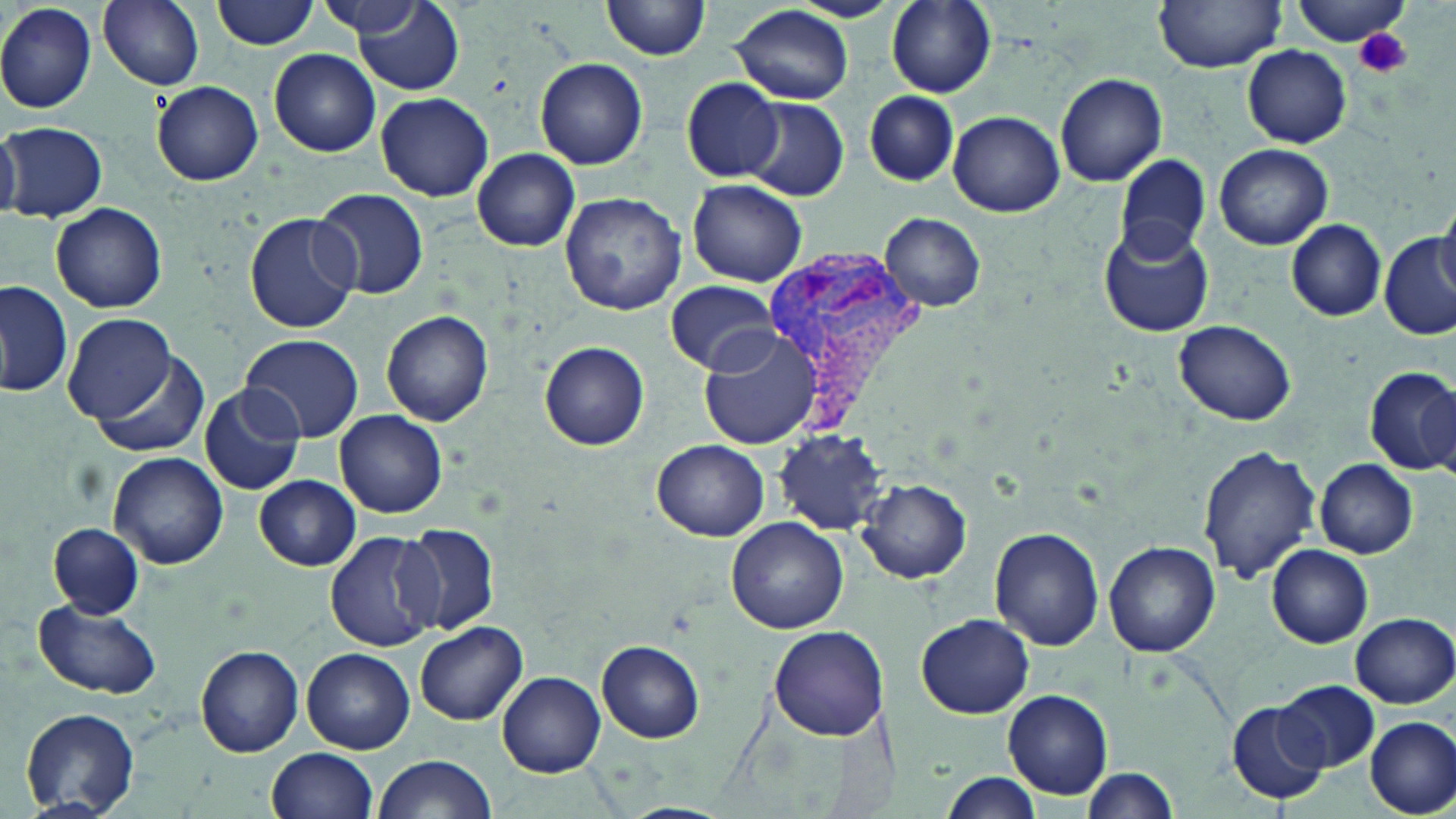

Summary:
  - Coordinate format: approximate bounding boxes as (x1,y1)-(x2,y2) corner pairs in pixels
  - Platelet locations: (1355,26)-(1411,78)
  - Uninfected red blood cell locations: (98,0)-(204,90), (213,0)-(318,50), (603,0)-(713,61), (885,0)-(996,98), (1154,0)-(1286,71), (1292,0)-(1414,47), (874,1)-(975,183), (0,2)-(97,113), (317,2)-(430,38), (352,3)-(464,97), (729,5)-(855,106), (1244,46)-(1351,147), (270,49)-(381,158), (535,57)-(647,169), (1055,72)-(1168,186), (681,78)-(784,181), (153,81)-(263,185), (376,92)-(493,201), (866,92)-(956,186), (741,99)-(848,200), (950,110)-(1064,216), (0,121)-(21,223), (2,122)-(108,223), (1213,143)-(1332,250), (471,148)-(580,251), (1117,154)-(1210,260), (687,179)-(807,287), (312,187)-(430,300), (561,193)-(687,316), (50,203)-(167,313), (1434,205)-(1456,303), (243,210)-(360,334), (882,214)-(986,312), (1286,219)-(1387,322), (1098,224)-(1213,338), (1381,234)-(1456,341), (666,281)-(780,374), (0,282)-(74,400), (381,310)-(493,426), (63,314)-(177,425), (1172,319)-(1300,423), (698,330)-(821,449), (239,333)-(363,442), (540,341)-(649,451), (85,350)-(211,461), (1362,365)-(1456,476), (198,385)-(305,496), (335,410)-(447,518), (774,428)-(890,534), (653,438)-(770,540), (1199,445)-(1320,581), (109,453)-(229,569), (1314,459)-(1418,558), (253,476)-(361,570), (856,476)-(972,583), (726,517)-(849,635), (398,522)-(499,636), (49,523)-(144,618), (990,527)-(1103,650), (326,531)-(441,653), (1103,540)-(1219,656), (1266,545)-(1374,648), (34,600)-(163,700), (1348,612)-(1456,708), (916,613)-(1034,719), (414,619)-(526,725), (769,625)-(889,741), (598,640)-(704,742), (196,646)-(304,757), (302,648)-(415,753), (499,671)-(604,776), (1274,679)-(1380,773), (1001,688)-(1114,800), (1228,701)-(1328,805), (20,707)-(139,817), (1367,718)-(1455,815), (268,747)-(378,819), (372,754)-(497,819), (1079,767)-(1182,816), (939,775)-(1045,818), (621,804)-(735,819)
  - Plasmodium vivax-infected red blood cell locations: (761,244)-(929,428)
  - Slide-level diagnosis: Plasmodium vivax
  - Image size: 1456×819 pixels
  - Stain: May-Grünwald-Giemsa
  - Field of view: one of a larger specimen
  - Modality: light microscopy
  - Preparation: thin blood film
  - Magnification: 1000x